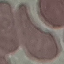

result = no malaria parasites seen
stain = Giemsa
preparation = thin blood film
image type = cell patch, automatically extracted from a larger field of view and resized to 64 × 64 pixels
capture = smartphone camera at the microscope eyepiece